Name the parasite shown.
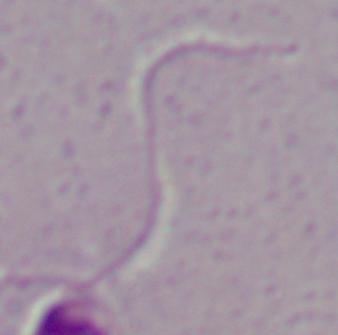
Leishmania.

{
  "modality": "micrograph",
  "magnification": "1000x"
}